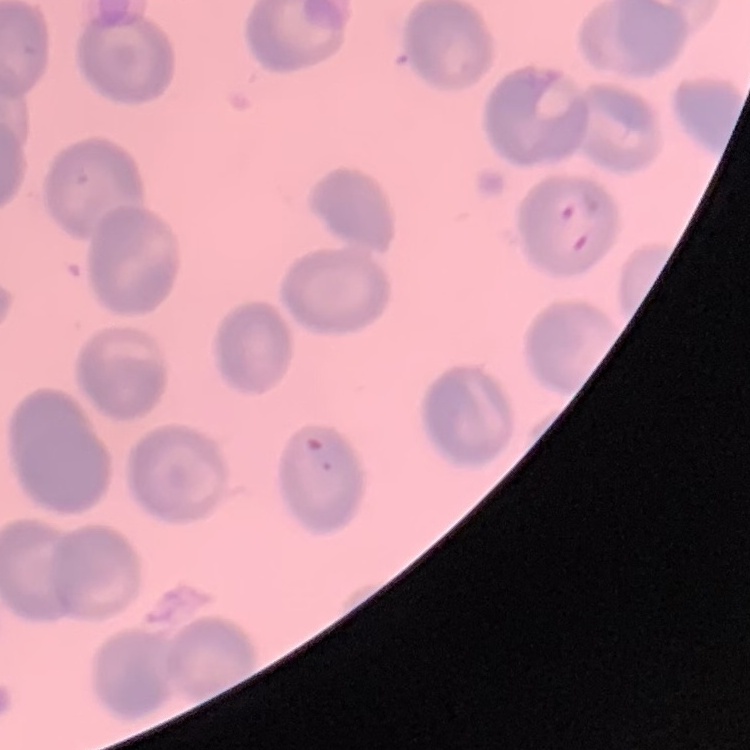
{
  "red_blood_cell_morphology": "no rouleaux formation",
  "preparation": "thin blood smear",
  "stain": "Field's or Giemsa",
  "image_type": "one tile cut from a larger photomicrograph"
}